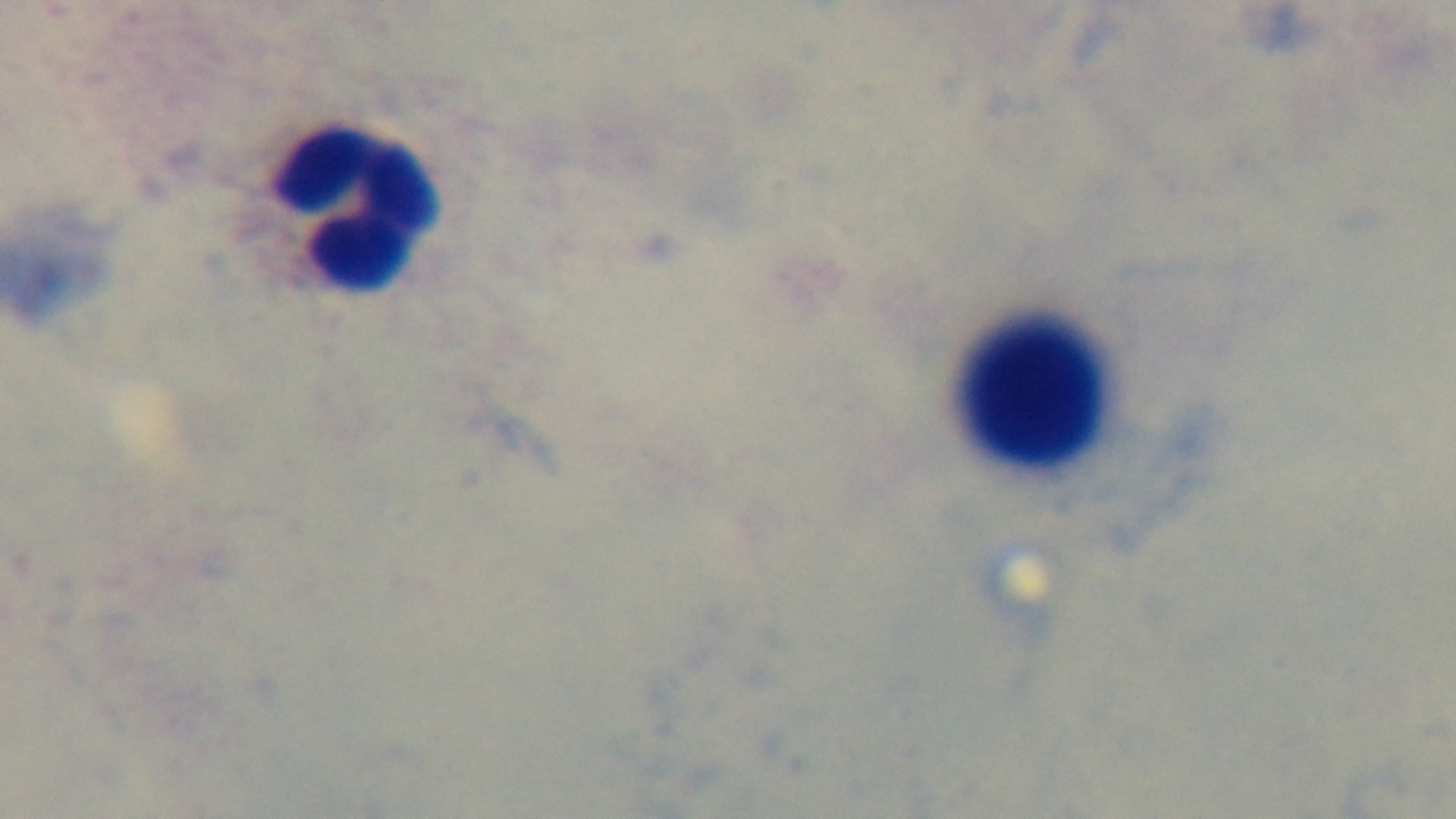

malaria status = negative
preparation = thick
modality = light microscopy
field of view = single
stain = Giemsa
objective = 100x oil immersion
capture = mounted 4K digital camera